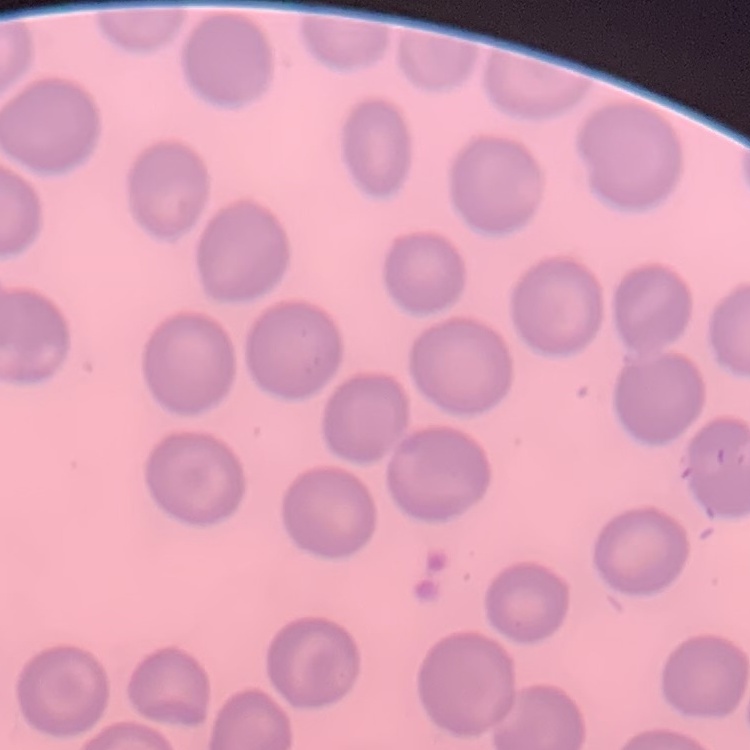

red blood cell morphology = no rouleaux formation
preparation = thin blood smear
stain = Field's or Giemsa
image type = square crop of a larger photomicrograph